Identify the parasite.
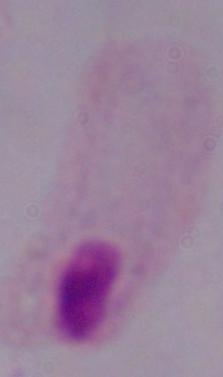
A trichomonad.

Micrograph. Captured at 1000x magnification.